Give the position of every leukocyte visible.
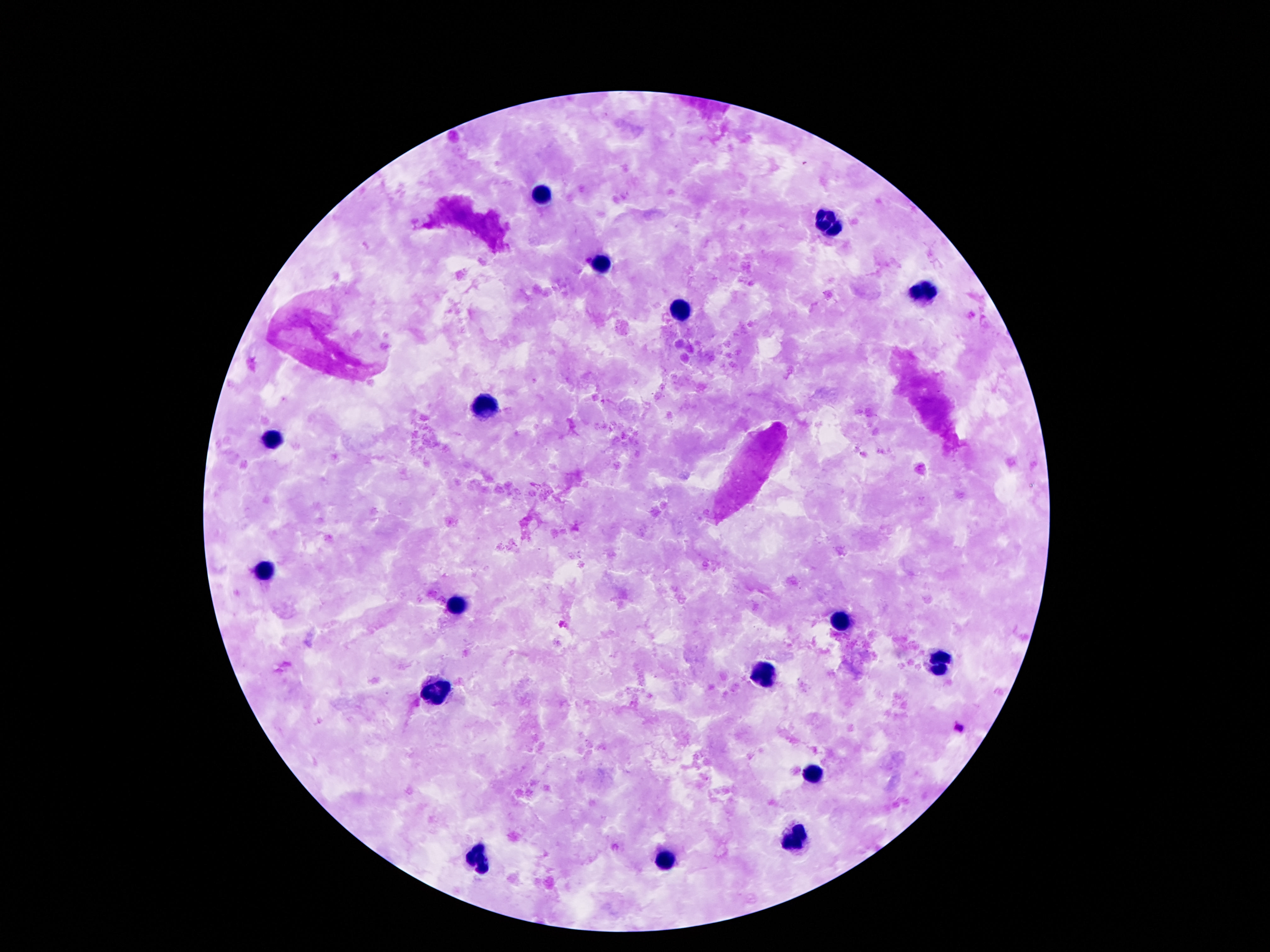
Approximate object centers, in pixels from the top-left corner.
Leukocytes: (x=538, y=192), (x=832, y=222), (x=604, y=265), (x=918, y=290), (x=681, y=306), (x=484, y=405), (x=272, y=441), (x=265, y=572), (x=457, y=605), (x=844, y=624), (x=939, y=666), (x=767, y=673), (x=433, y=690), (x=813, y=774), (x=793, y=838), (x=477, y=859), (x=669, y=860).

patient malaria status = not infected
stain = Giemsa
image size = 1270×952 pixels
preparation = thick blood smear
magnification = 100x
field of view = one from this slide
capture = smartphone camera through the microscope eyepiece